Report the malaria status of this cell.
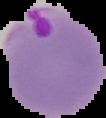
Parasitized.

Summary:
  - Image size: 106×118 pixels
  - Image type: cell region segmented out of the field of view; surrounding area masked to black
  - Preparation: thin blood smear